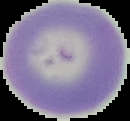

{
  "preparation": "thin blood film",
  "malaria_status": "uninfected",
  "image_size": "130×121 pixels",
  "image_type": "segmented cell region with the area outside set to black"
}